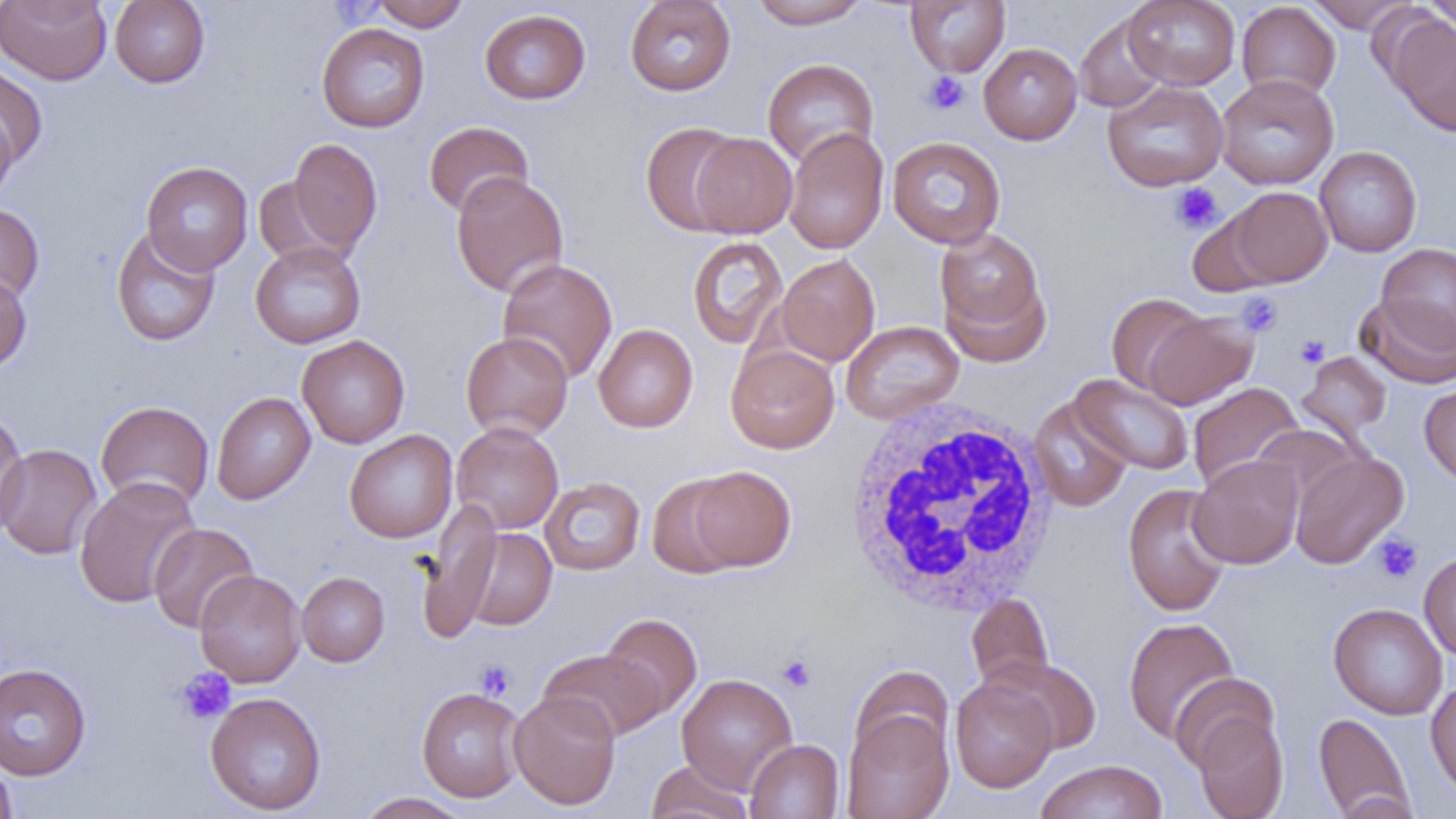

slide-level diagnosis = no evidence of blood parasites
field of view = single
uninfected red blood cell locations = approximate bounding boxes as [x1, y1, x2, y2] in pixels: [109, 0, 210, 88], [370, 0, 470, 31], [749, 0, 870, 29], [1123, 0, 1240, 90], [1304, 0, 1416, 32], [1423, 0, 1456, 38], [0, 1, 111, 85], [624, 1, 736, 96], [906, 1, 1010, 77], [1236, 2, 1341, 101], [480, 9, 591, 104], [1074, 13, 1168, 113], [1383, 13, 1456, 136], [316, 23, 430, 133], [979, 43, 1082, 145], [762, 58, 879, 167], [0, 66, 48, 168], [1215, 74, 1339, 190], [1102, 80, 1229, 191], [0, 108, 17, 207], [422, 121, 533, 218], [640, 122, 746, 236], [783, 127, 889, 255], [689, 132, 798, 238], [887, 136, 1006, 249], [288, 138, 383, 253], [1314, 146, 1422, 257], [141, 161, 253, 275], [450, 170, 569, 297], [252, 177, 345, 265], [1225, 186, 1333, 287], [0, 202, 45, 305], [1186, 211, 1280, 298], [111, 226, 221, 347], [934, 228, 1052, 364], [686, 236, 788, 349], [250, 241, 366, 348], [1376, 243, 1456, 350], [776, 254, 880, 366], [497, 258, 618, 384], [0, 271, 31, 373], [1106, 293, 1211, 395], [1357, 293, 1456, 389], [1143, 310, 1258, 410], [841, 320, 964, 424], [593, 324, 698, 432], [460, 331, 573, 440], [296, 335, 410, 448], [726, 344, 840, 454], [1297, 352, 1392, 441], [1068, 374, 1194, 476], [1187, 382, 1305, 493], [1419, 383, 1456, 487], [211, 392, 316, 504], [1029, 396, 1133, 512], [95, 400, 214, 511], [0, 409, 29, 537], [451, 421, 563, 534], [344, 429, 458, 543], [0, 442, 102, 560], [1290, 450, 1409, 568], [1189, 455, 1304, 568], [685, 466, 796, 572], [646, 473, 748, 578], [74, 476, 201, 608], [539, 476, 645, 575], [1122, 483, 1233, 617], [417, 501, 502, 642], [148, 522, 259, 634], [461, 528, 557, 630], [1419, 550, 1456, 662], [194, 569, 306, 687], [296, 571, 390, 667], [966, 593, 1054, 691], [1328, 602, 1448, 719], [600, 613, 702, 720], [1123, 617, 1240, 743], [537, 647, 668, 741], [986, 655, 1102, 754], [0, 662, 91, 780], [850, 664, 955, 766], [676, 673, 798, 794], [1170, 673, 1280, 772], [950, 676, 1057, 793], [1425, 677, 1456, 799], [416, 686, 526, 802], [204, 691, 327, 815], [509, 691, 621, 809], [841, 708, 954, 819], [1192, 712, 1289, 819], [1314, 712, 1414, 819], [745, 739, 844, 819], [0, 756, 17, 819], [1033, 759, 1169, 819], [645, 761, 754, 819], [356, 792, 474, 818]
white blood cell locations = approximate bounding boxes as [x1, y1, x2, y2] in pixels: [840, 398, 1059, 620]
platelet locations = approximate bounding boxes as [x1, y1, x2, y2] in pixels: [921, 71, 971, 115], [1171, 182, 1222, 233], [1235, 292, 1283, 337], [1295, 334, 1330, 367], [1373, 533, 1422, 583], [777, 654, 817, 692], [475, 659, 516, 701], [176, 667, 236, 724]
magnification = 1000x
image size = 1456×819 pixels
preparation = thin blood smear
modality = optical microscopy